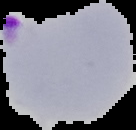

malaria status = parasitized
image size = 136×130 pixels
preparation = thin blood smear
image type = segmented cell region on a black background